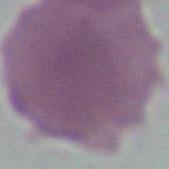
Summary:
  - Modality: micrograph
  - Identification: erythrocyte
  - Magnification: 1000x